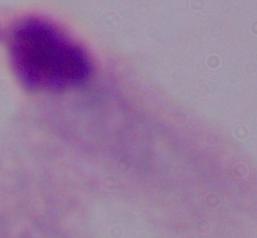

Micrograph. Captured at 1000x magnification. A trichomonad is shown.